Report the malaria status of this cell.
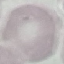
Uninfected.

Automatically extracted cell patch, resized to 64 × 64 pixels. Acquired by smartphone through the microscope eyepiece. Giemsa stain. Thin blood film.